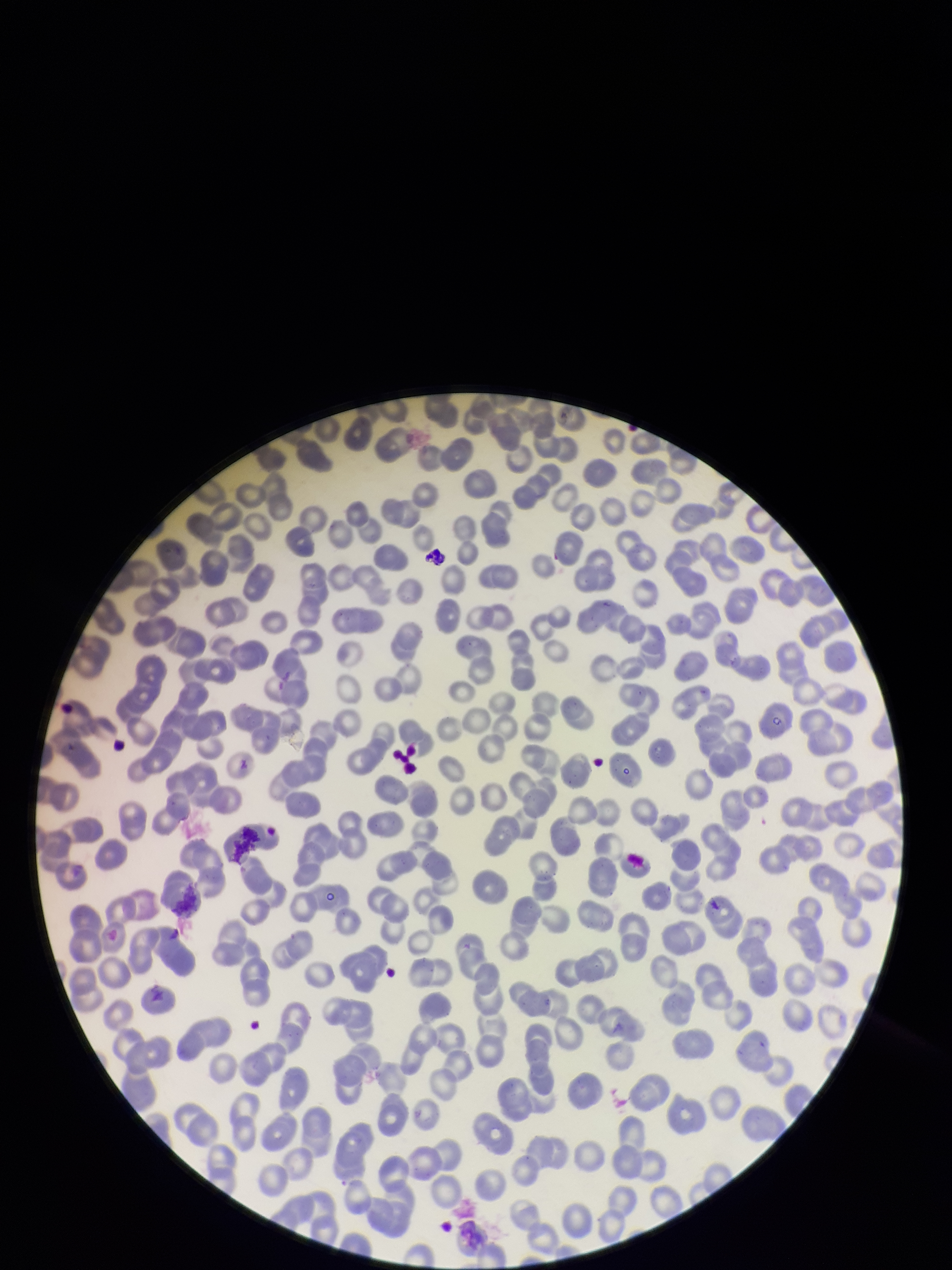

red_blood_cell_count: 256
image_size: 952×1270 pixels
parasitized_red_blood_cells: none identified
patient_malaria_status: negative
capture: smartphone photograph through the microscope eyepiece
parasitized_red_blood_cell_count: 0
preparation: thin smear
stain: Giemsa
field_of_view: single